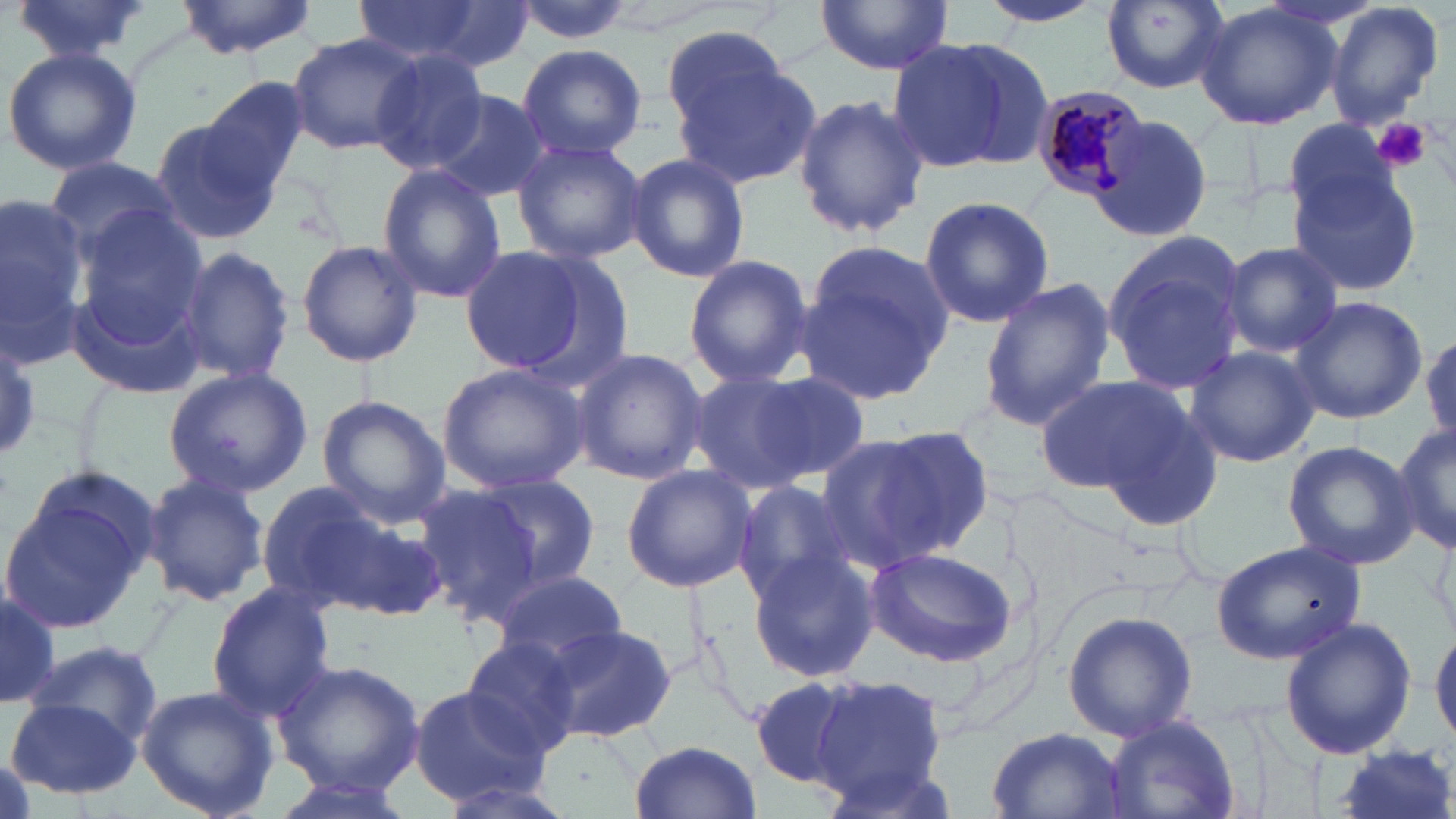 Approximate bounding boxes as [x1, y1, x2, y2] in pixels. Plasmodium malariae-infected red blood cell locations: [1030, 84, 1149, 202]. Uninfected red blood cell locations: [8, 0, 157, 63], [174, 0, 319, 58], [352, 0, 518, 69], [506, 0, 639, 47], [978, 0, 1110, 31], [1323, 0, 1445, 132], [814, 1, 955, 73], [1099, 2, 1229, 92], [1195, 3, 1344, 131], [660, 23, 794, 136], [287, 33, 421, 155], [887, 35, 1053, 175], [516, 43, 647, 161], [2, 44, 144, 175], [668, 45, 822, 193], [367, 50, 489, 173], [199, 79, 314, 197], [430, 89, 553, 203], [792, 93, 928, 240], [1094, 115, 1217, 244], [149, 119, 282, 245], [1279, 119, 1405, 227], [509, 137, 647, 263], [624, 153, 750, 284], [44, 154, 185, 260], [376, 165, 507, 305], [1287, 168, 1424, 294], [0, 193, 93, 367], [917, 193, 1057, 328], [66, 207, 211, 373], [1099, 228, 1252, 394], [295, 237, 424, 369], [798, 239, 956, 403], [457, 243, 603, 378], [1221, 243, 1344, 357], [176, 244, 295, 390], [684, 253, 813, 389], [977, 279, 1116, 431], [1289, 295, 1429, 426], [1422, 328, 1456, 451], [0, 333, 42, 460], [1182, 345, 1321, 467], [569, 348, 708, 486], [436, 362, 589, 494], [161, 367, 314, 500], [685, 369, 820, 496], [745, 371, 873, 486], [1034, 375, 1192, 496], [316, 396, 450, 525], [1094, 403, 1223, 533], [1393, 421, 1455, 557], [816, 429, 979, 575], [1282, 440, 1420, 572], [621, 463, 755, 594], [0, 469, 163, 637], [139, 472, 269, 608], [469, 475, 602, 588], [250, 479, 423, 618], [410, 480, 563, 625], [731, 480, 857, 602], [1427, 515, 1456, 646], [1212, 540, 1366, 664], [863, 545, 1019, 667], [745, 548, 881, 683], [488, 571, 629, 671], [205, 583, 336, 722], [1, 586, 62, 712], [1062, 609, 1199, 743], [1278, 615, 1418, 761], [539, 623, 678, 744], [1432, 626, 1456, 745], [460, 636, 585, 758], [26, 638, 163, 748], [273, 659, 426, 795], [748, 674, 865, 790], [811, 675, 947, 801], [136, 684, 279, 819], [406, 684, 551, 808], [7, 694, 142, 799], [1104, 717, 1243, 819], [986, 727, 1131, 819], [629, 739, 762, 819], [1330, 746, 1456, 819], [266, 775, 415, 819], [431, 775, 581, 819]. Platelet locations: [1376, 118, 1431, 174]. Slide-level diagnosis: Plasmodium malariae. One field of a larger specimen. Optical microscopy. Image is 1456×819 pixels. Captured at 1000x magnification. May-Grünwald-Giemsa-stained preparation. Thin blood smear.